Comment on the morphology of the erythrocytes.
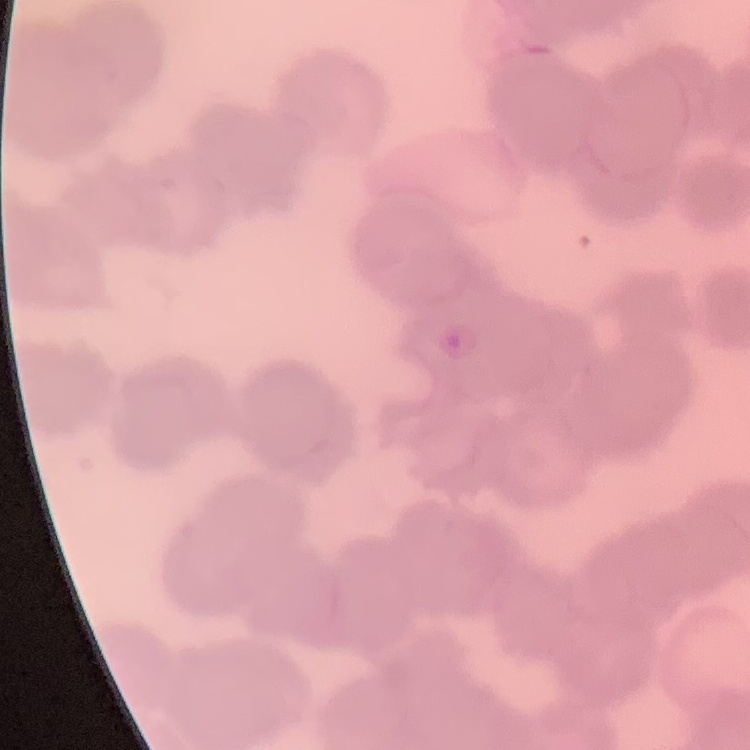
Rouleaux formation.

Summary:
  - Image type: square crop of a larger photomicrograph
  - Preparation: thin blood film
  - Stain: Field's or Giemsa